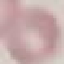

Summary:
  - Result: negative for malaria parasites
  - Stain: Giemsa
  - Capture: smartphone camera at the microscope eyepiece
  - Preparation: thin smear
  - Image type: cell patch, automatically extracted from a larger field of view and resized to 64 × 64 pixels